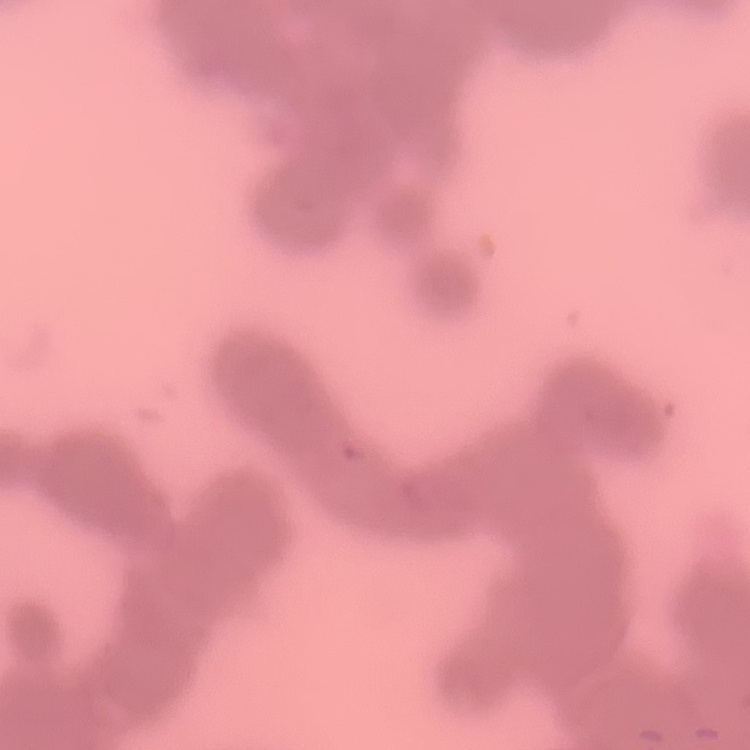

red_blood_cell_morphology: rouleaux formation
stain: Field's or Giemsa
image_type: one tile cut from a larger photomicrograph
preparation: thin blood film